Report the malaria status of this cell.
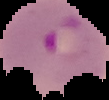
It is parasitized.

Image is 109×100 pixels. Cell region segmented out of the field of view; the surrounding area is masked to black. From a thin blood film.